Give the extent of all Plasmodium falciparum-infected red blood cells.
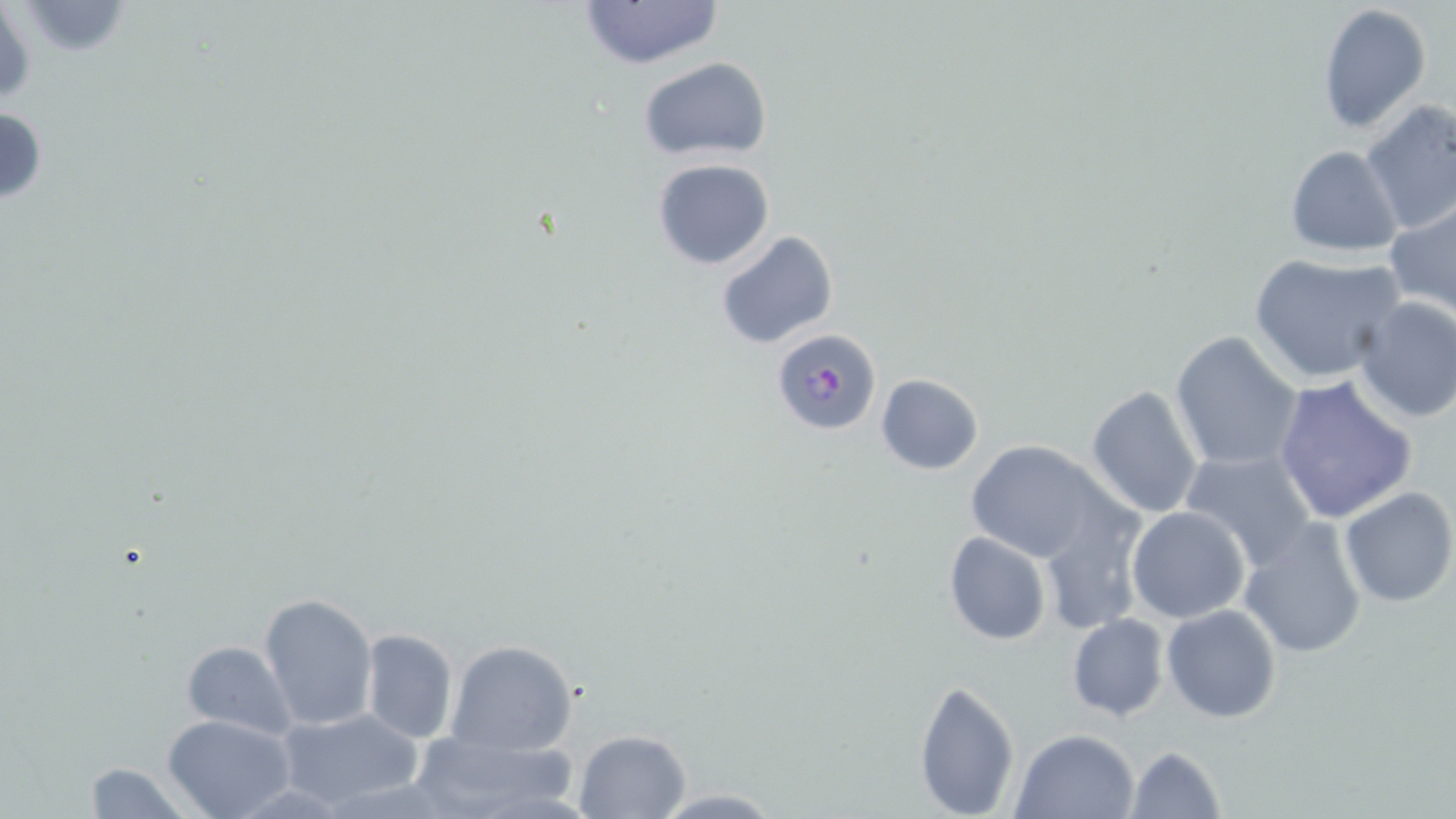
Approximate bounding boxes as (x1, y1, x2, y2) in pixels.
Plasmodium falciparum-infected red blood cells: (771, 329, 881, 436).

Summary:
  - Uninfected red blood cell locations: (575, 0, 726, 69), (1, 2, 35, 112), (17, 2, 135, 56), (1317, 4, 1433, 133), (639, 57, 771, 163), (1360, 101, 1456, 237), (1, 107, 48, 205), (1284, 146, 1404, 259), (652, 159, 776, 271), (672, 195, 814, 339), (1383, 201, 1456, 320), (716, 231, 839, 351), (1248, 252, 1405, 384), (1350, 294, 1456, 425), (1170, 331, 1306, 472), (876, 374, 984, 475), (1273, 376, 1419, 525), (1085, 384, 1203, 520), (961, 441, 1109, 565), (1179, 448, 1319, 572), (1339, 486, 1455, 607), (1037, 499, 1144, 635), (1126, 506, 1251, 623), (1237, 518, 1367, 659), (943, 532, 1051, 645), (259, 592, 378, 729), (1161, 603, 1282, 724), (1067, 615, 1168, 721), (360, 629, 457, 744), (180, 639, 296, 739), (445, 639, 579, 755), (913, 677, 1020, 818), (277, 706, 426, 813), (162, 714, 295, 819), (573, 728, 691, 818), (1011, 728, 1139, 818), (409, 729, 583, 818), (1125, 744, 1227, 819), (78, 761, 191, 819), (648, 786, 789, 817)
  - Slide-level diagnosis: Plasmodium falciparum
  - Magnification: 1000x
  - Image size: 1456×819 pixels
  - Preparation: thin blood film
  - Field of view: single
  - Modality: light microscopy
  - Stain: May-Grünwald-Giemsa